Identify the preparation type.
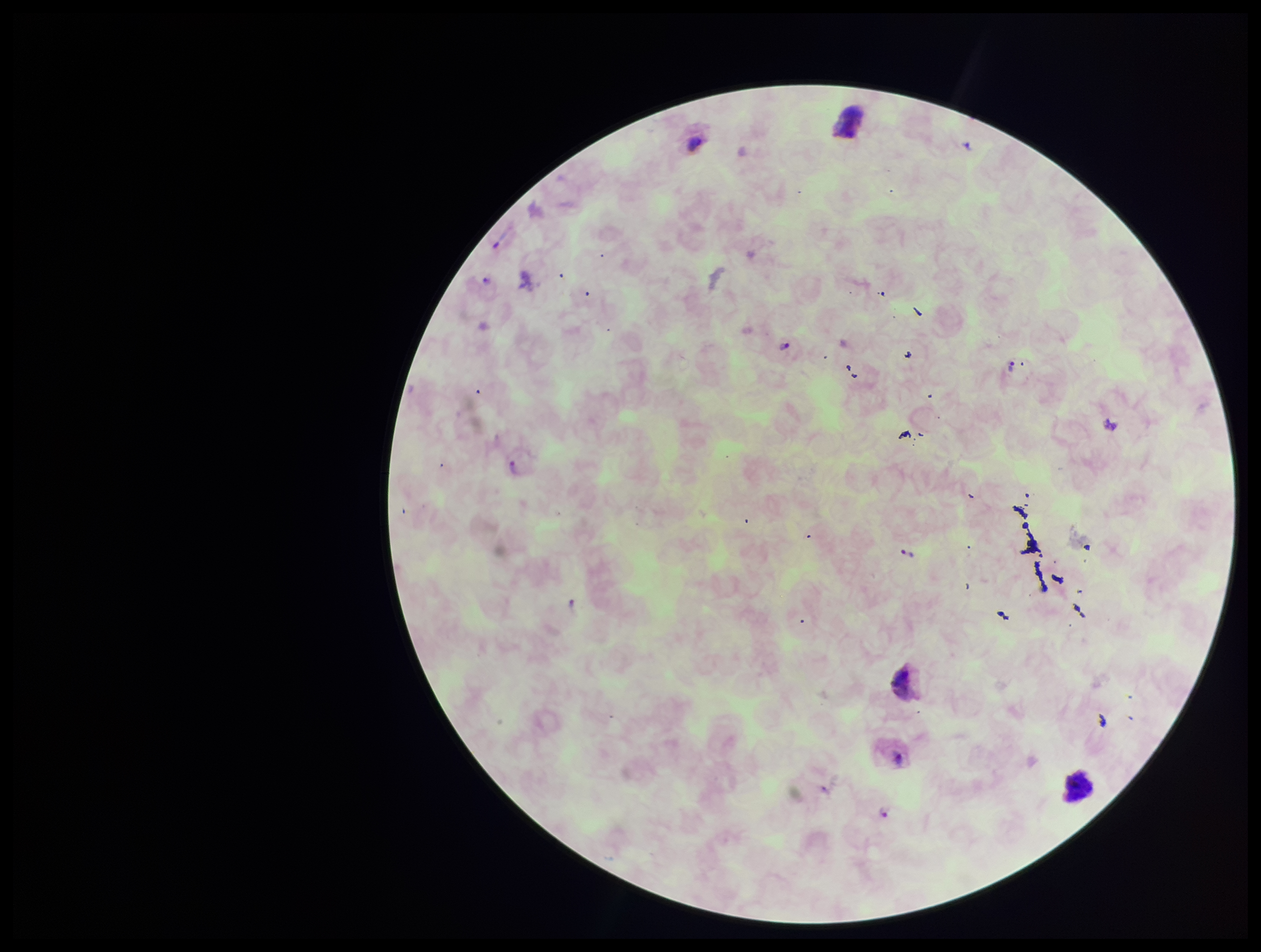
A thick smear.

stain = Giemsa
field of view = one from this slide
leukocyte count = 1
species reported for this patient = Plasmodium vivax
Plasmodium parasites = identified
parasite count = 6
patient malaria status = positive
capture = smartphone photograph through the microscope eyepiece
image size = 1261×952 pixels